Assess this cell for malaria.
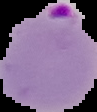

It is parasitized.

{
  "preparation": "thin blood smear",
  "image_size": "97×112 pixels",
  "image_type": "segmented cell region with the area outside set to black"
}